Report the malaria status of this cell.
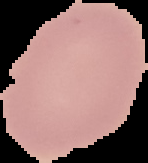

Uninfected.

image_size: 148×163 pixels
image_type: segmented cell region with the area outside set to black
preparation: thin blood smear